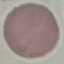

Summary:
  - Malaria status: uninfected
  - Preparation: thin blood film
  - Stain: Giemsa
  - Capture: smartphone camera at the microscope eyepiece
  - Image type: cell patch, automatically extracted from a larger field of view and resized to 64 × 64 pixels